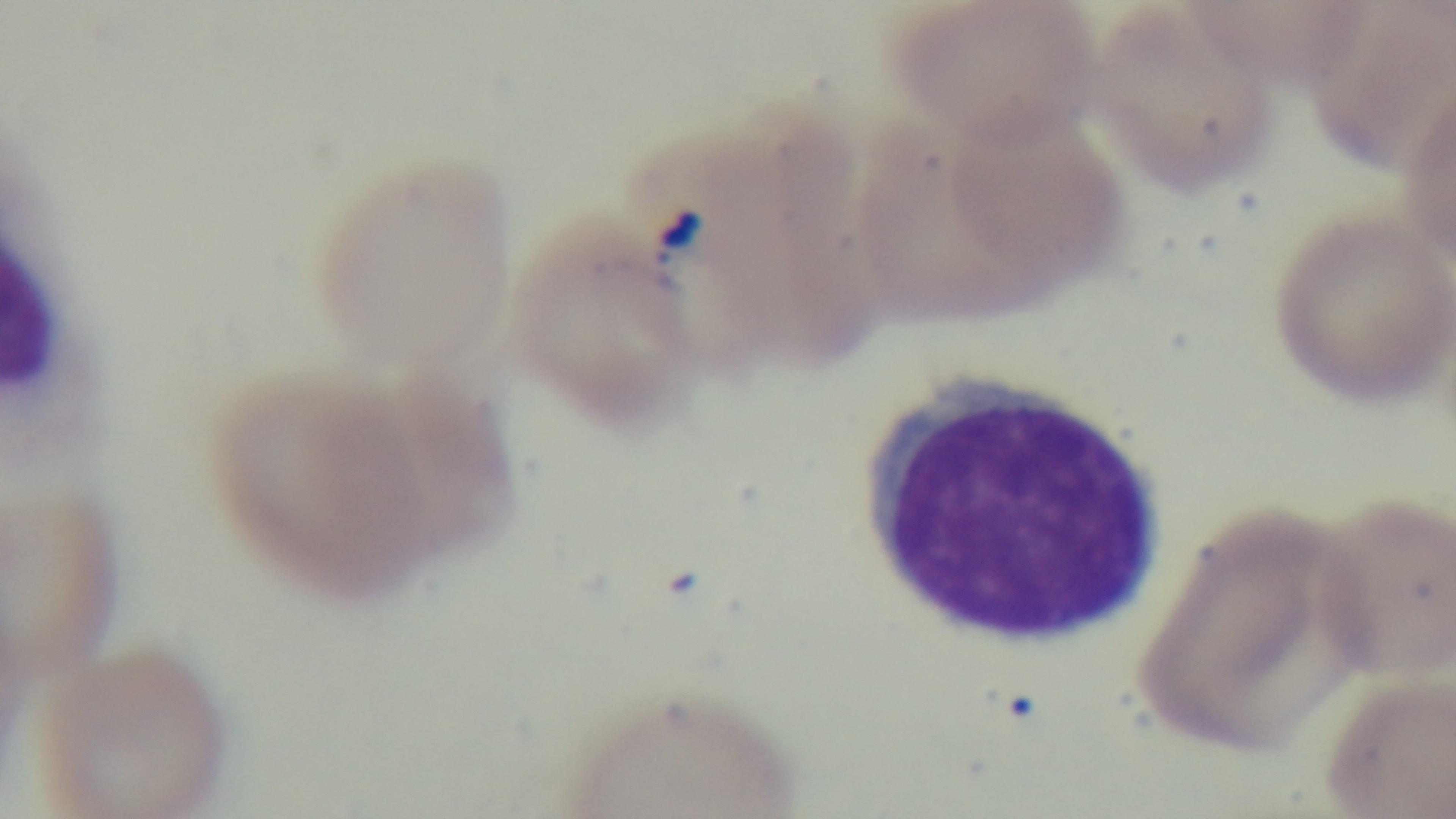

objective = 100x oil immersion
malaria status = positive
modality = light microscopy
stain = Giemsa
preparation = thin blood film
capture = mounted 4K digital camera
field of view = single